Locate every blood parasite and identify its species.
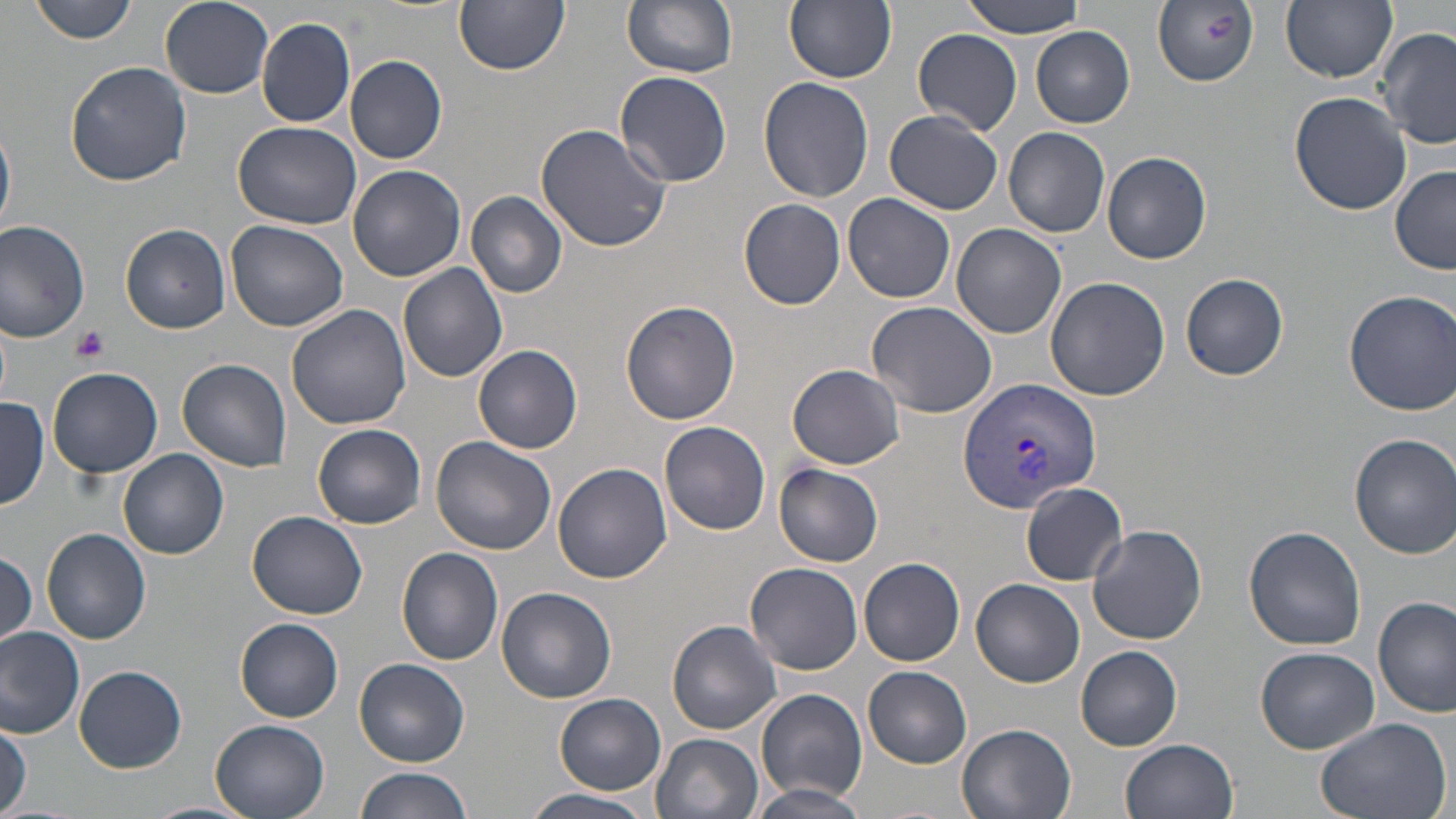
Approximate bounding boxes as named x1/y1/x2/y2 corners in pixels.
Plasmodium vivax-infected red blood cells: (x1=957, y1=376, x2=1102, y2=511).
No Plasmodium falciparum, Plasmodium ovale, Plasmodium malariae, Babesia divergens, or Trypanosoma brucei observed.

Summary:
  - Uninfected red blood cell locations: (x1=28, y1=0, x2=142, y2=44), (x1=455, y1=0, x2=570, y2=75), (x1=622, y1=0, x2=738, y2=78), (x1=785, y1=0, x2=897, y2=84), (x1=960, y1=0, x2=1088, y2=39), (x1=1282, y1=0, x2=1396, y2=84), (x1=160, y1=2, x2=275, y2=99), (x1=1152, y1=2, x2=1261, y2=87), (x1=256, y1=17, x2=356, y2=128), (x1=1379, y1=27, x2=1456, y2=150), (x1=1030, y1=28, x2=1135, y2=128), (x1=913, y1=29, x2=1024, y2=134), (x1=345, y1=55, x2=448, y2=164), (x1=66, y1=61, x2=192, y2=187), (x1=615, y1=71, x2=733, y2=187), (x1=758, y1=77, x2=875, y2=203), (x1=1288, y1=91, x2=1411, y2=215), (x1=885, y1=111, x2=1004, y2=215), (x1=0, y1=119, x2=15, y2=237), (x1=234, y1=122, x2=365, y2=230), (x1=534, y1=122, x2=672, y2=251), (x1=1003, y1=127, x2=1111, y2=238), (x1=1102, y1=150, x2=1211, y2=264), (x1=347, y1=165, x2=466, y2=281), (x1=1390, y1=165, x2=1455, y2=274), (x1=466, y1=191, x2=569, y2=299), (x1=844, y1=193, x2=956, y2=306), (x1=739, y1=198, x2=846, y2=309), (x1=0, y1=219, x2=94, y2=343), (x1=225, y1=221, x2=348, y2=332), (x1=121, y1=222, x2=232, y2=333), (x1=952, y1=223, x2=1066, y2=338), (x1=398, y1=263, x2=510, y2=384), (x1=1181, y1=273, x2=1288, y2=381), (x1=1045, y1=276, x2=1169, y2=400), (x1=1344, y1=289, x2=1455, y2=415), (x1=620, y1=300, x2=742, y2=426), (x1=866, y1=301, x2=997, y2=419), (x1=288, y1=305, x2=413, y2=430), (x1=473, y1=344, x2=583, y2=454), (x1=176, y1=358, x2=293, y2=472), (x1=786, y1=363, x2=907, y2=470), (x1=47, y1=368, x2=164, y2=478), (x1=0, y1=398, x2=48, y2=510), (x1=659, y1=420, x2=772, y2=536), (x1=312, y1=423, x2=426, y2=529), (x1=1350, y1=434, x2=1456, y2=558), (x1=431, y1=435, x2=558, y2=554), (x1=120, y1=448, x2=230, y2=561), (x1=553, y1=463, x2=671, y2=583), (x1=773, y1=464, x2=884, y2=566), (x1=1021, y1=481, x2=1127, y2=585), (x1=245, y1=509, x2=367, y2=620), (x1=1088, y1=524, x2=1208, y2=645), (x1=1243, y1=525, x2=1367, y2=651), (x1=42, y1=527, x2=153, y2=644), (x1=396, y1=547, x2=504, y2=667), (x1=0, y1=552, x2=37, y2=650), (x1=860, y1=558, x2=965, y2=666), (x1=743, y1=562, x2=863, y2=675), (x1=972, y1=579, x2=1084, y2=687), (x1=496, y1=586, x2=616, y2=704), (x1=1373, y1=596, x2=1455, y2=717), (x1=237, y1=618, x2=344, y2=722), (x1=667, y1=619, x2=782, y2=733), (x1=0, y1=627, x2=85, y2=738), (x1=1075, y1=646, x2=1183, y2=750), (x1=1254, y1=646, x2=1382, y2=753), (x1=353, y1=658, x2=469, y2=765), (x1=75, y1=665, x2=186, y2=772), (x1=863, y1=666, x2=972, y2=767), (x1=756, y1=688, x2=868, y2=802), (x1=554, y1=694, x2=666, y2=794), (x1=1311, y1=715, x2=1452, y2=819), (x1=208, y1=718, x2=329, y2=819), (x1=0, y1=720, x2=29, y2=813), (x1=957, y1=723, x2=1077, y2=819), (x1=651, y1=731, x2=762, y2=819), (x1=1119, y1=738, x2=1238, y2=819), (x1=353, y1=765, x2=474, y2=819), (x1=748, y1=783, x2=870, y2=819), (x1=524, y1=789, x2=659, y2=819), (x1=142, y1=800, x2=254, y2=819)
  - Platelet locations: (x1=70, y1=324, x2=110, y2=363)
  - Slide-level diagnosis: Plasmodium vivax
  - Image size: 1456×819 pixels
  - Field of view: one of a larger specimen
  - Stain: May-Grünwald-Giemsa
  - Modality: optical microscopy
  - Magnification: 1000x
  - Preparation: thin blood smear